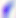
{
  "magnification": "400x",
  "modality": "micrograph",
  "identification": "Toxoplasma gondii"
}